Identify the parasite.
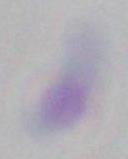
Toxoplasma gondii.

magnification: 1000x
modality: photomicrograph